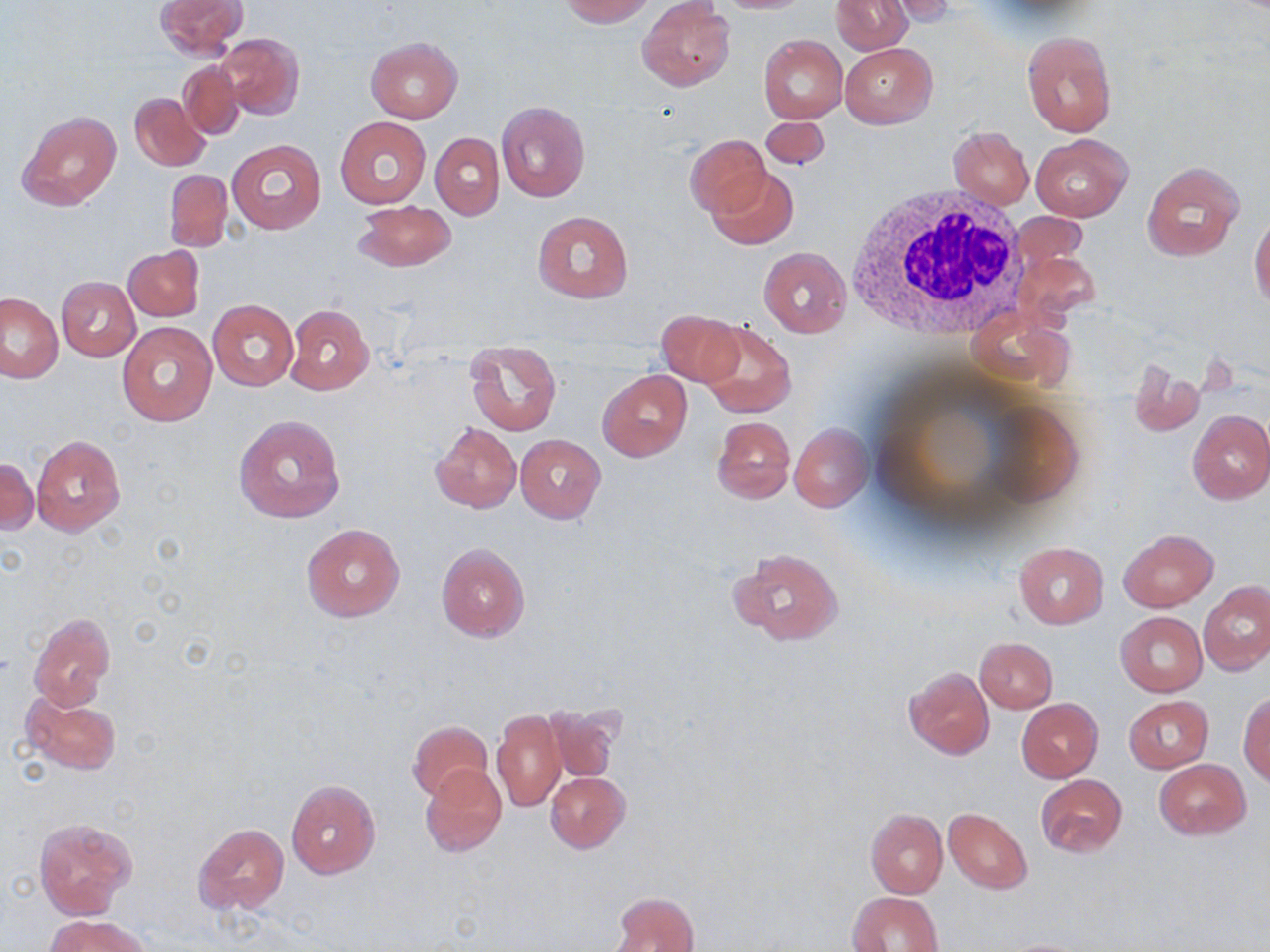

slide-level diagnosis = negative for blood parasites
stain = May-Grünwald-Giemsa
preparation = thin blood smear
modality = light microscopy
field of view = single
uninfected red blood cell locations = approximate bounding boxes as named x1/y1/x2/y2 corners in pixels: (x1=154, y1=0, x2=246, y2=58), (x1=560, y1=0, x2=655, y2=26), (x1=831, y1=0, x2=912, y2=54), (x1=638, y1=1, x2=734, y2=91), (x1=879, y1=1, x2=956, y2=26), (x1=1022, y1=30, x2=1115, y2=137), (x1=215, y1=33, x2=304, y2=121), (x1=758, y1=34, x2=847, y2=123), (x1=365, y1=37, x2=462, y2=122), (x1=839, y1=43, x2=936, y2=128), (x1=178, y1=61, x2=243, y2=139), (x1=130, y1=91, x2=209, y2=170), (x1=495, y1=101, x2=591, y2=202), (x1=16, y1=108, x2=122, y2=210), (x1=335, y1=116, x2=430, y2=209), (x1=758, y1=116, x2=831, y2=173), (x1=948, y1=126, x2=1034, y2=209), (x1=431, y1=132, x2=504, y2=221), (x1=1030, y1=134, x2=1132, y2=221), (x1=686, y1=136, x2=770, y2=216), (x1=228, y1=139, x2=326, y2=234), (x1=1142, y1=162, x2=1243, y2=262), (x1=709, y1=168, x2=798, y2=250), (x1=164, y1=170, x2=232, y2=250), (x1=353, y1=200, x2=455, y2=271), (x1=532, y1=210, x2=633, y2=303), (x1=1249, y1=213, x2=1270, y2=311), (x1=124, y1=246, x2=203, y2=322), (x1=759, y1=246, x2=851, y2=336), (x1=57, y1=277, x2=140, y2=360), (x1=1, y1=293, x2=65, y2=382), (x1=207, y1=299, x2=299, y2=391), (x1=285, y1=304, x2=374, y2=394), (x1=657, y1=308, x2=745, y2=387), (x1=698, y1=319, x2=796, y2=417), (x1=117, y1=322, x2=217, y2=426), (x1=465, y1=338, x2=561, y2=437), (x1=1128, y1=361, x2=1204, y2=437), (x1=599, y1=370, x2=691, y2=460), (x1=1187, y1=409, x2=1270, y2=504), (x1=233, y1=413, x2=346, y2=525), (x1=710, y1=415, x2=795, y2=504), (x1=430, y1=421, x2=521, y2=513), (x1=790, y1=423, x2=871, y2=512), (x1=31, y1=435, x2=127, y2=536), (x1=514, y1=435, x2=605, y2=522), (x1=0, y1=456, x2=37, y2=536), (x1=300, y1=524, x2=407, y2=622), (x1=1118, y1=528, x2=1218, y2=610), (x1=1014, y1=541, x2=1109, y2=628), (x1=434, y1=542, x2=531, y2=642), (x1=728, y1=547, x2=845, y2=647), (x1=1199, y1=583, x2=1270, y2=676), (x1=1115, y1=612, x2=1207, y2=697), (x1=29, y1=614, x2=118, y2=709), (x1=974, y1=637, x2=1057, y2=714), (x1=903, y1=667, x2=995, y2=758), (x1=20, y1=692, x2=122, y2=774), (x1=1239, y1=692, x2=1270, y2=785), (x1=1124, y1=696, x2=1215, y2=772), (x1=1016, y1=699, x2=1102, y2=782), (x1=541, y1=704, x2=620, y2=784), (x1=491, y1=708, x2=566, y2=813), (x1=408, y1=721, x2=492, y2=803), (x1=1154, y1=758, x2=1251, y2=839), (x1=421, y1=765, x2=506, y2=857), (x1=545, y1=772, x2=630, y2=852), (x1=1035, y1=774, x2=1126, y2=856), (x1=286, y1=779, x2=380, y2=877), (x1=865, y1=809, x2=948, y2=897), (x1=943, y1=809, x2=1033, y2=893), (x1=33, y1=817, x2=135, y2=919), (x1=193, y1=822, x2=289, y2=915), (x1=609, y1=891, x2=698, y2=952), (x1=848, y1=891, x2=944, y2=951), (x1=48, y1=916, x2=149, y2=952), (x1=995, y1=937, x2=1095, y2=951)
magnification = 1000x
image size = 1270×952 pixels
white blood cell locations = approximate bounding boxes as named x1/y1/x2/y2 corners in pixels: (x1=843, y1=184, x2=1030, y2=337)